Assess this cell for malaria.
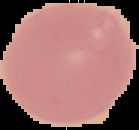
Uninfected.

The area outside the segmented cell region is set to black. Image is 139×130 pixels. From a thin blood smear.